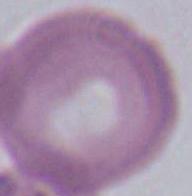
Summary:
  - Magnification: 1000x
  - Modality: micrograph
  - Identification: red blood cell